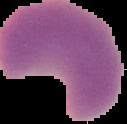
From a thin blood smear. Image is 127×124 pixels. Cell region segmented out of the field of view; the surrounding area is masked to black. Malaria status: parasitized.